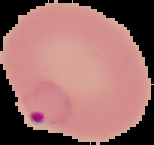 Cell region segmented out of the field of view; the surrounding area is masked to black. From a thin blood film. Malaria status: parasitized. Image is 154×145 pixels.